Name the parasite shown.
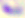
This is Toxoplasma gondii.

magnification = 400x
modality = photomicrograph